Identify the preparation type.
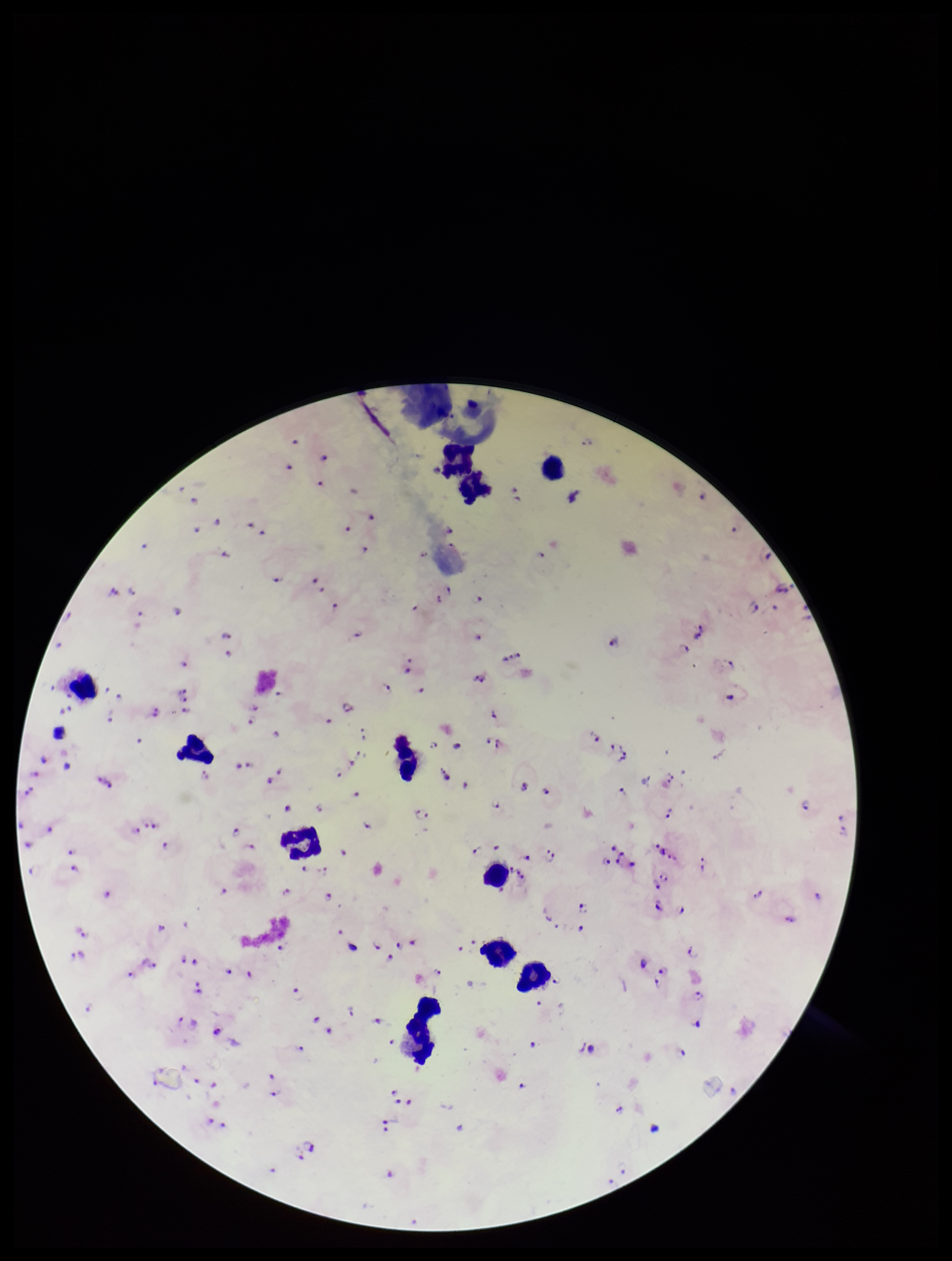
A thick smear.

Plasmodium parasites: detected. Image is 952×1261 pixels. Leukocyte count: 11. Photographed through the microscope eyepiece with a smartphone camera. Single field of view. Species reported for this patient: Plasmodium falciparum. Parasite count: 98. Patient malaria status: infected. Giemsa stain.